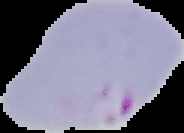

Summary:
  - Preparation: thin blood film
  - Malaria status: parasitized
  - Image type: segmented cell region with the area outside set to black
  - Image size: 184×133 pixels